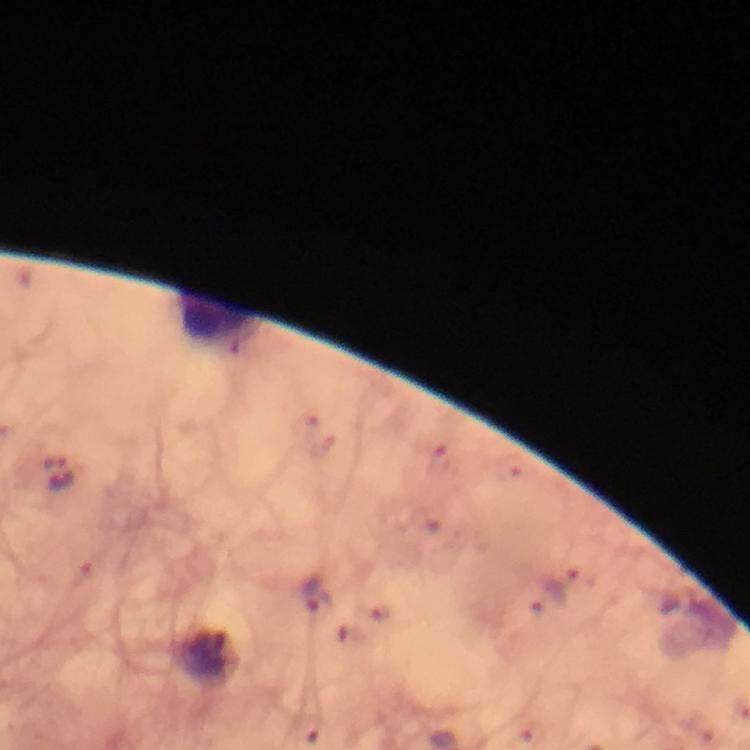

{
  "leukocyte_locations": "approximate centers as {x, y} in pixels: {218, 317}",
  "magnification": "100x",
  "stain": "Giemsa",
  "capture": "smartphone photograph through a microscope",
  "preparation": "thick smear",
  "plasmodium_parasite_locations": "approximate centers as {x, y} in pixels: {442, 462}, {56, 463}, {563, 585}, {314, 594}",
  "immersion_oil": "used",
  "image_size": "750×750 pixels",
  "context": "from a malaria diagnostic workup",
  "cropped_from": "a single field of view"
}